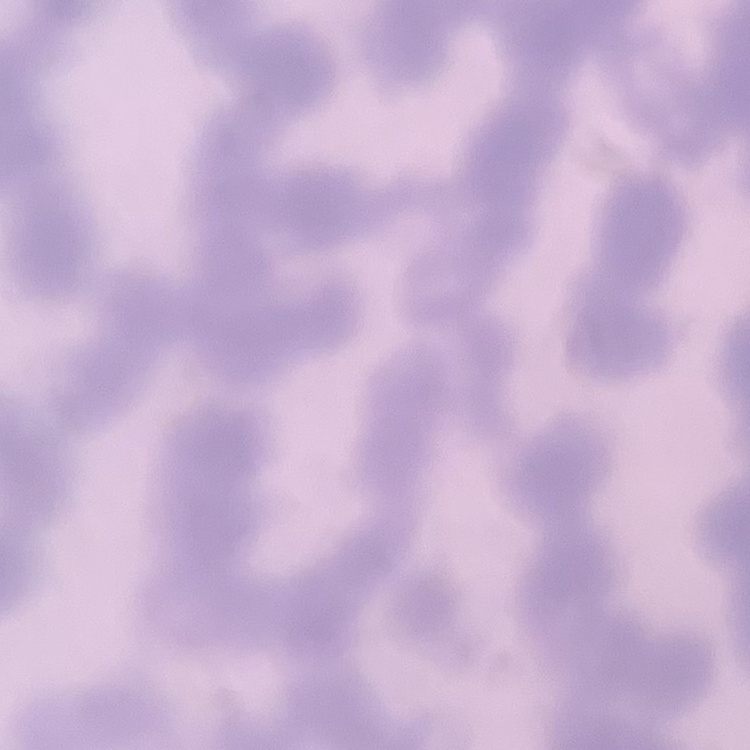

{
  "red_blood_cell_morphology": "rouleaux formation",
  "stain": "Field's or Giemsa",
  "image_type": "one tile cut from a larger photomicrograph",
  "preparation": "thin blood smear"
}